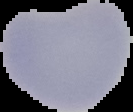
The area outside the segmented cell region is set to black. From a thin blood film. Malaria status: parasitized. Image is 133×112 pixels.